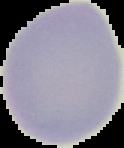

Segmented cell region on a black background. From a thin blood film. Malaria status: uninfected. Image is 124×148 pixels.